Outline each blood parasite and name the species.
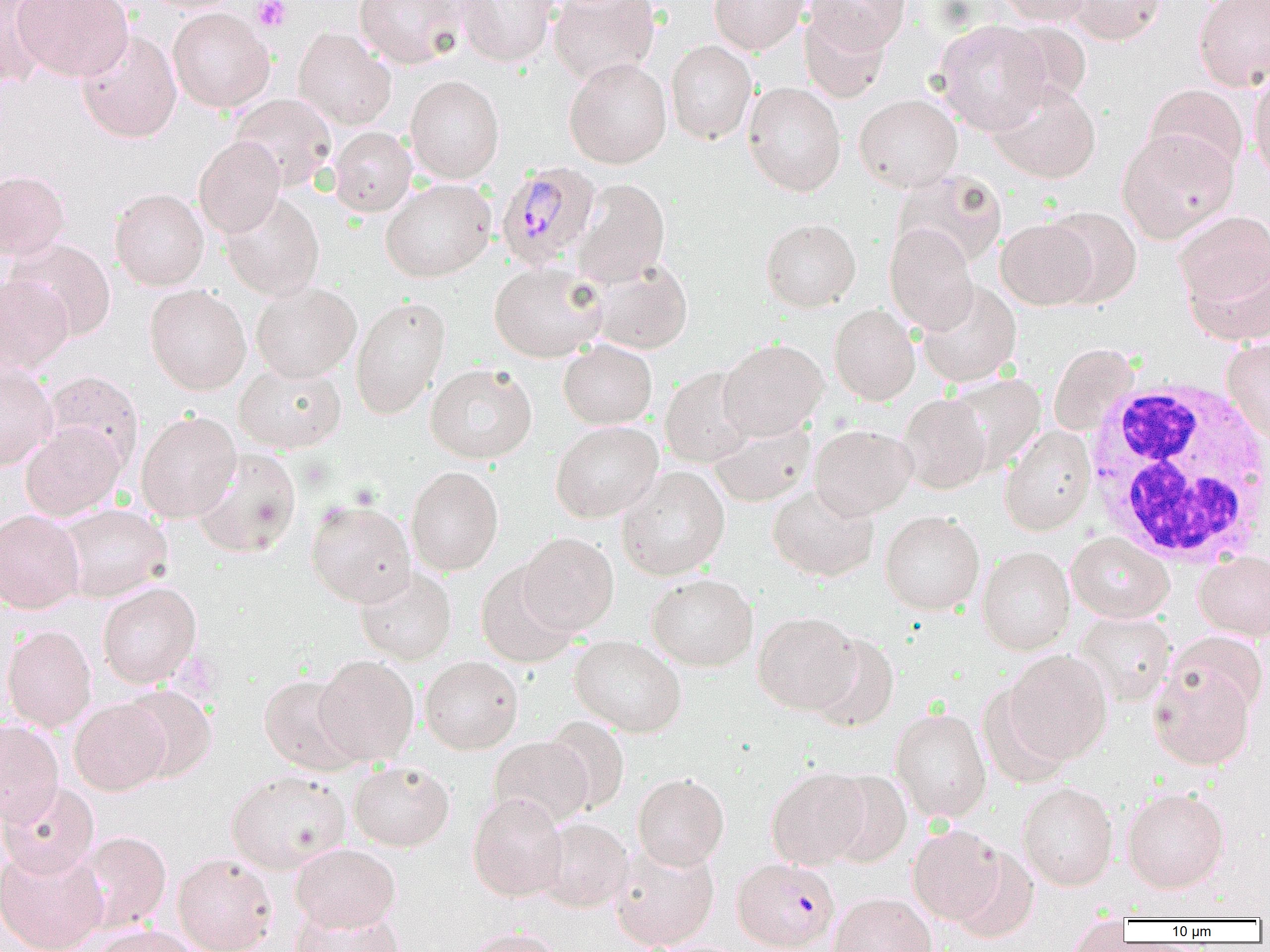

Approximate bounding boxes as (x1,y1)-(x2,y2) corner pairs in pixels.
Plasmodium malariae-infected red blood cells: (495,161)-(602,270), (731,857)-(840,952).
No Plasmodium falciparum, Plasmodium ovale, Plasmodium vivax, Babesia divergens, or Trypanosoma brucei observed.

White blood cell locations: (1081,376)-(1270,567). Uninfected red blood cell locations: (1,0)-(56,87), (13,0)-(134,81), (141,0)-(246,13), (354,0)-(465,68), (455,0)-(559,67), (549,0)-(660,85), (709,0)-(809,55), (805,0)-(910,53), (995,0)-(1094,26), (1063,0)-(1167,45), (1193,0)-(1270,91), (167,7)-(275,113), (799,7)-(891,103), (933,20)-(1052,135), (1001,21)-(1091,110), (293,27)-(395,130), (77,30)-(182,143), (665,40)-(757,144), (564,57)-(672,168), (1249,70)-(1270,181), (405,75)-(504,183), (988,81)-(1101,183), (743,82)-(846,196), (1144,84)-(1249,179), (230,93)-(337,191), (854,94)-(963,192), (329,126)-(417,217), (1117,130)-(1238,243), (193,136)-(286,238), (0,169)-(70,261), (893,169)-(1008,269), (380,178)-(496,282), (572,178)-(670,287), (110,188)-(209,290), (220,193)-(325,301), (1043,206)-(1142,308), (1174,211)-(1270,309), (760,218)-(860,312), (996,218)-(1097,310), (884,223)-(978,333), (6,238)-(117,342), (1183,253)-(1270,346), (589,259)-(693,355), (489,261)-(607,361), (0,272)-(72,377), (917,280)-(1022,388), (251,281)-(361,381), (145,284)-(251,395), (350,296)-(450,419), (829,304)-(920,405), (1222,338)-(1270,443), (558,339)-(657,429), (718,339)-(828,440), (1049,343)-(1138,436), (235,362)-(346,454), (0,363)-(58,470), (425,364)-(537,464), (660,366)-(757,468), (43,371)-(144,472), (945,373)-(1046,473), (898,393)-(993,494), (136,410)-(241,523), (707,417)-(815,508), (551,421)-(663,523), (20,422)-(126,521), (809,424)-(917,520), (1000,425)-(1096,535), (192,449)-(301,558), (405,466)-(504,576), (617,466)-(730,580), (767,483)-(879,582), (306,500)-(416,607), (55,503)-(173,602), (0,509)-(85,614), (879,510)-(985,614), (518,532)-(618,634), (1066,532)-(1174,623), (977,546)-(1075,655), (1194,550)-(1270,641), (475,562)-(579,668), (355,567)-(457,665), (646,573)-(758,671), (97,581)-(201,688), (753,611)-(860,714), (1075,611)-(1176,706), (2,624)-(97,731), (1167,632)-(1268,720), (807,633)-(899,732), (570,635)-(687,737), (1005,650)-(1112,764), (314,655)-(418,765), (420,656)-(523,754), (1149,661)-(1256,770), (258,674)-(363,776), (976,683)-(1074,790), (120,685)-(218,783), (69,697)-(170,795), (891,707)-(992,823), (542,716)-(630,815), (0,719)-(64,827), (489,736)-(593,828), (348,761)-(455,852), (766,767)-(871,869), (226,769)-(351,873), (824,770)-(912,867), (632,773)-(729,871), (0,781)-(100,879), (1017,782)-(1118,890), (1122,787)-(1230,893), (467,792)-(567,901), (536,817)-(634,913), (908,824)-(1009,927), (74,831)-(172,933), (609,842)-(720,950), (290,843)-(401,932), (0,845)-(108,952), (950,847)-(1040,943), (172,853)-(278,952), (829,892)-(936,952), (289,906)-(406,952), (1066,918)-(1135,951), (87,925)-(202,952), (463,927)-(565,952). Platelet locations: (252,0)-(291,31). Slide-level diagnosis: Plasmodium malariae. Thin blood film. One field of a larger specimen. Light microscopy. Image is 1270×952 pixels. 1000x magnification.